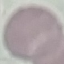

Summary:
  - Malaria status: uninfected
  - Preparation: thin blood smear
  - Image type: automatically extracted cell patch, resized to 64 × 64 pixels
  - Stain: Giemsa
  - Capture: smartphone camera at the microscope eyepiece